Draw a bounding box around every Plasmodium parasite.
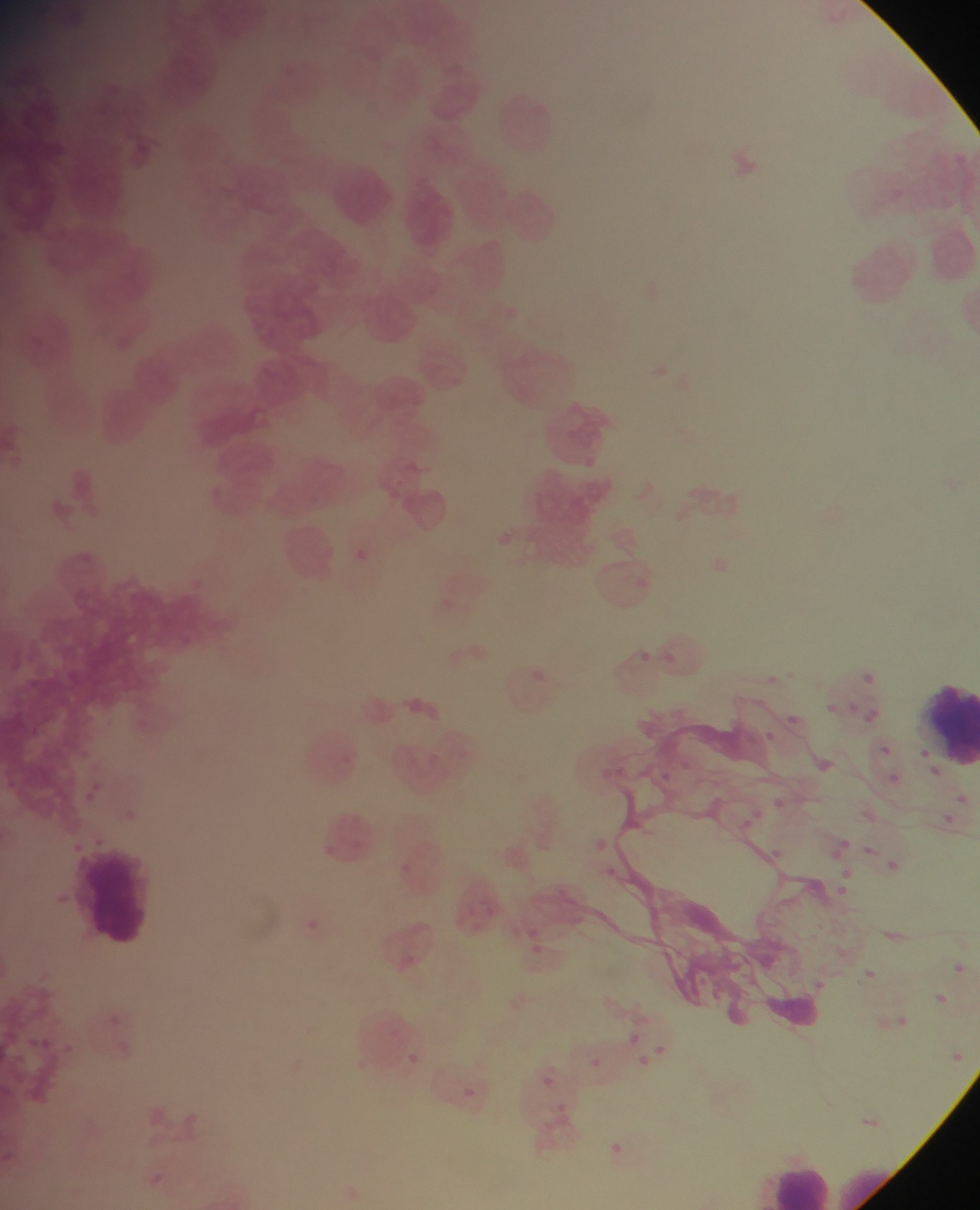

Approximate bounding boxes as {left, top, right, bottom} in pixels.
Plasmodium parasites: {952, 151, 969, 167}, {498, 525, 530, 570}, {349, 547, 380, 567}, {635, 642, 657, 666}, {670, 646, 690, 664}, {860, 662, 879, 688}, {757, 665, 789, 694}, {530, 666, 555, 688}, {826, 687, 839, 714}, {850, 694, 868, 724}, {866, 700, 890, 729}, {789, 707, 808, 728}, {763, 728, 787, 757}, {877, 742, 894, 759}, {662, 747, 695, 774}, {884, 770, 905, 786}, {87, 773, 109, 807}, {775, 788, 787, 804}, {956, 793, 970, 806}, {119, 802, 145, 827}, {743, 804, 774, 826}, {943, 806, 958, 833}, {830, 830, 852, 850}, {760, 839, 778, 863}, {863, 841, 881, 862}, {883, 851, 912, 885}, {391, 858, 431, 887}, {597, 859, 619, 884}, {837, 867, 858, 903}, {477, 890, 513, 924}, {292, 911, 331, 945}, {519, 937, 550, 968}, {854, 958, 875, 982}, {948, 960, 967, 977}, {809, 975, 818, 990}, {929, 989, 949, 1008}, {109, 1003, 132, 1023}, {891, 1011, 913, 1031}, {26, 1027, 56, 1052}, {622, 1027, 643, 1051}, {66, 1039, 88, 1063}, {649, 1041, 671, 1061}, {395, 1046, 426, 1074}, {946, 1047, 966, 1066}, {583, 1054, 607, 1076}, {542, 1067, 553, 1082}, {455, 1081, 483, 1105}, {863, 1112, 879, 1131}, {159, 1113, 185, 1135}, {599, 1134, 631, 1160}, {148, 1166, 171, 1186}.

{
  "leukocyte_locations": "approximate bounding boxes as {left, top, right, bottom} in pixels: {485, 87, 569, 163}, {323, 162, 401, 234}, {912, 678, 980, 769}, {74, 844, 160, 948}, {752, 1150, 843, 1210}",
  "capture": "mobile-phone photograph through a microscope",
  "image_size": "980×1210 pixels",
  "preparation": "thin blood smear",
  "country": "Ghana",
  "field_of_view": "single"
}